State the blood parasite species.
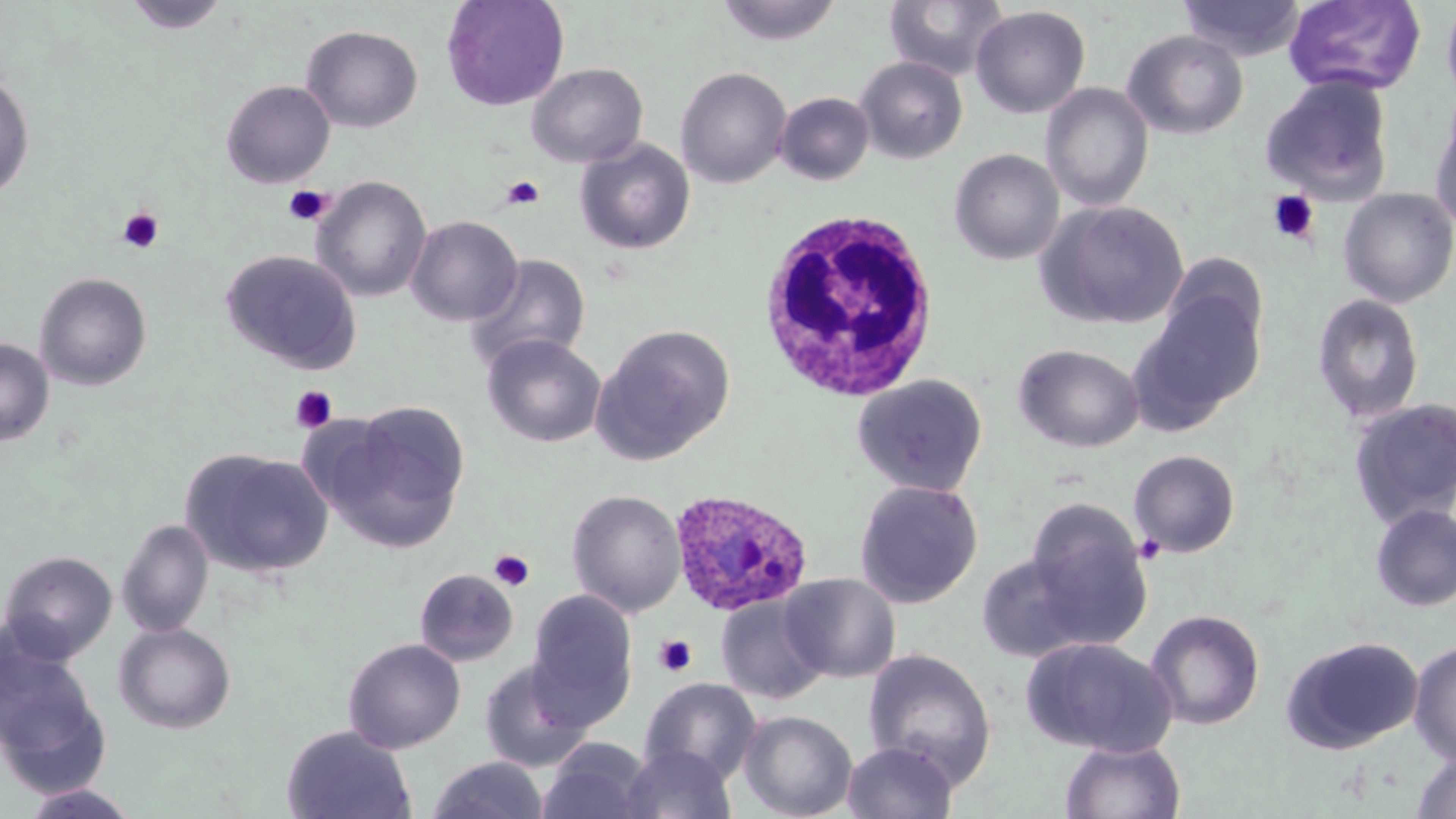

Plasmodium ovale.

Approximate bounding boxes as [x1, y1, x2, y2] in pixels. Uninfected red blood cell locations: [122, 0, 231, 35], [441, 0, 569, 112], [883, 0, 1009, 81], [1179, 0, 1306, 61], [1284, 0, 1427, 96], [1441, 0, 1456, 111], [716, 1, 842, 46], [971, 5, 1090, 119], [301, 25, 423, 133], [1122, 29, 1249, 140], [856, 56, 968, 164], [526, 63, 648, 168], [676, 66, 792, 189], [0, 71, 35, 200], [1260, 75, 1395, 204], [221, 80, 335, 188], [1040, 83, 1154, 212], [774, 92, 875, 185], [1429, 102, 1456, 235], [574, 138, 696, 255], [949, 149, 1065, 265], [312, 176, 432, 302], [1337, 187, 1456, 307], [1037, 200, 1190, 330], [406, 216, 523, 326], [220, 250, 363, 374], [1157, 253, 1269, 357], [463, 254, 591, 373], [34, 272, 153, 391], [1131, 289, 1266, 427], [1311, 293, 1426, 424], [590, 323, 736, 465], [482, 333, 607, 448], [0, 338, 54, 447], [1013, 344, 1144, 453], [852, 374, 989, 496], [1348, 398, 1456, 527], [324, 401, 471, 551], [180, 448, 334, 579], [1128, 450, 1241, 558], [854, 480, 983, 609], [566, 489, 686, 617], [1023, 498, 1152, 645], [1370, 503, 1456, 612], [117, 519, 214, 638], [0, 550, 117, 664], [976, 553, 1094, 663], [414, 568, 519, 667], [781, 573, 901, 683], [525, 588, 637, 727], [715, 595, 830, 705], [1145, 609, 1265, 731], [114, 623, 236, 734], [0, 635, 107, 778], [1280, 635, 1424, 754], [1020, 637, 1176, 757], [343, 638, 466, 754], [1408, 640, 1456, 765], [862, 649, 997, 787], [478, 660, 595, 773], [640, 677, 762, 784], [738, 710, 858, 819], [281, 724, 417, 819], [1060, 738, 1186, 819], [538, 739, 654, 819], [841, 740, 959, 819], [621, 745, 736, 819], [1409, 751, 1456, 819], [427, 756, 548, 819], [19, 783, 141, 818]. White blood cell locations: [756, 207, 941, 401]. Plasmodium ovale-infected red blood cell locations: [669, 489, 813, 617]. Platelet locations: [501, 175, 545, 210], [284, 186, 333, 225], [1266, 190, 1320, 244], [116, 206, 165, 254], [290, 385, 338, 434], [488, 549, 535, 591], [654, 634, 697, 677]. Image is 1456×819 pixels. Single field of view. Captured at 1000x magnification. Thin blood smear. Light microscopy. May-Grünwald-Giemsa stain.